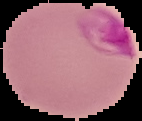

Summary:
  - Preparation: thin blood smear
  - Malaria status: parasitized
  - Image type: cell region segmented out of the field of view; surrounding area masked to black
  - Image size: 142×121 pixels